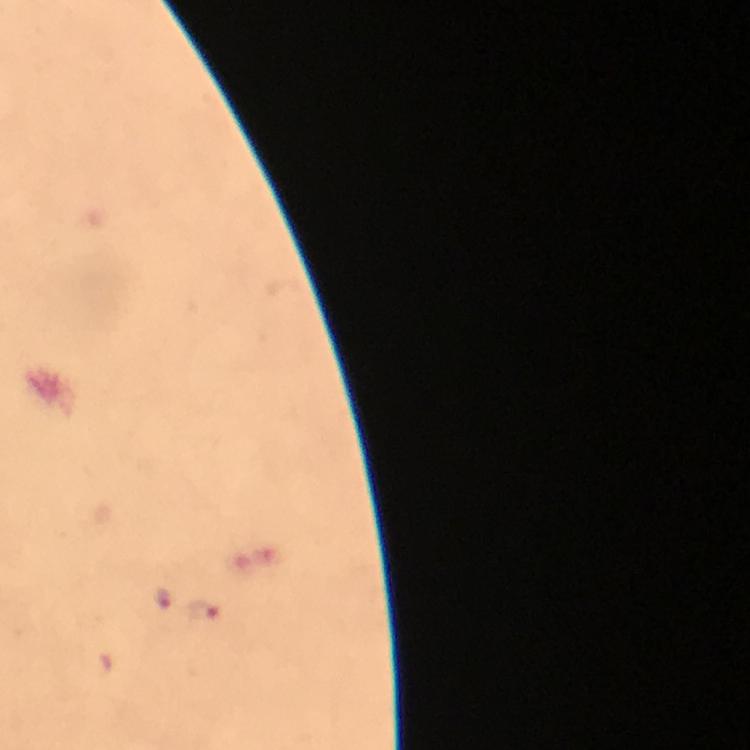

Approximate centers as {x, y} in pixels. Plasmodium parasite locations: {163, 598}, {202, 611}. Image is 750×750 pixels. From a malaria diagnostic workup. Photographed through the microscope with a smartphone camera. A crop from one field of view. Immersion oil was used. Thick blood film. At 100x magnification. Giemsa stain.